Report the malaria status of this cell.
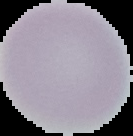

It is uninfected.

image_size: 133×136 pixels
image_type: cell region segmented out of the field of view; surrounding area masked to black
preparation: thin blood film